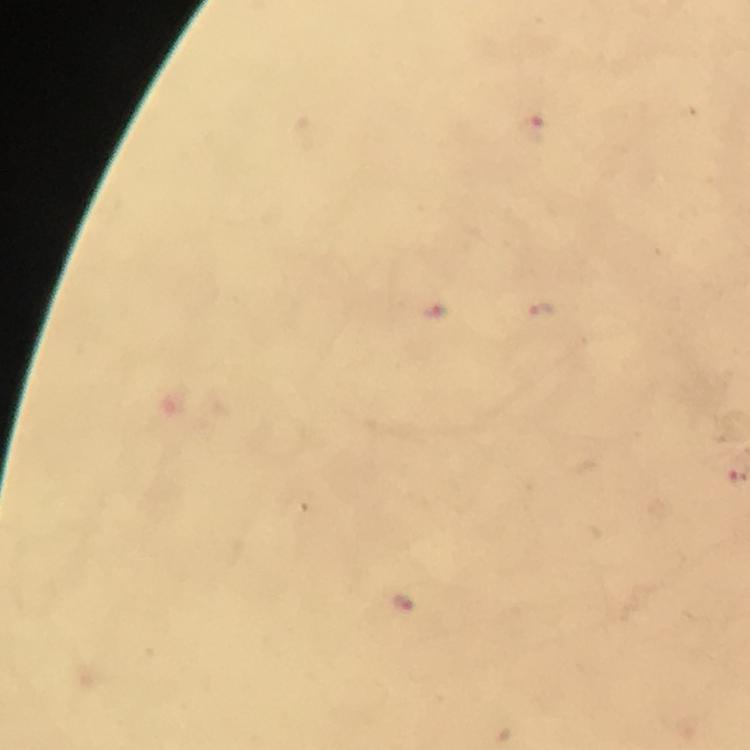

Approximate centers as (x, y) in pixels.
Summary:
  - Malaria parasite locations: (533, 130), (436, 310), (541, 310), (402, 602)
  - Context: from a diagnostic examination for malaria
  - Preparation: thick blood film
  - Magnification: 100x
  - Cropped from: one field of view
  - Stain: Giemsa
  - Image size: 750×750 pixels
  - Capture: smartphone photograph through a microscope
  - Immersion oil: applied